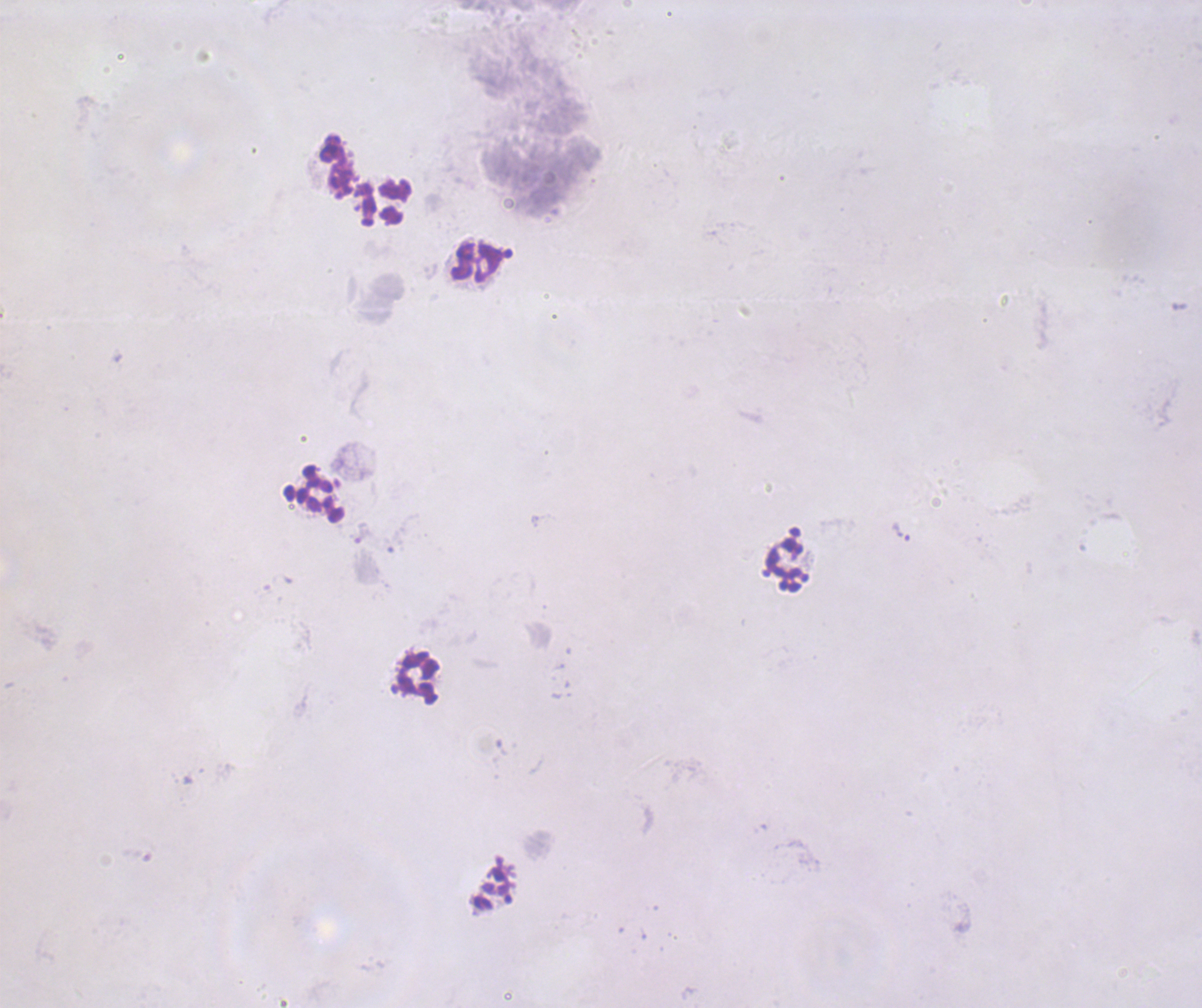
coordinate format = approximate centers as {x, y} in pixels
trophozoite locations = {900, 533}
leukocyte locations = {336, 166}, {386, 202}, {477, 263}, {315, 496}, {787, 565}, {417, 678}
stain = Romanowsky
field of view = single
image size = 1202×1008 pixels
context = previously used in an actual diagnosis
background quality = unsatisfactory
result = positive for Plasmodium parasites
magnification = 100x
preparation = thick blood smear
coloration quality = bad